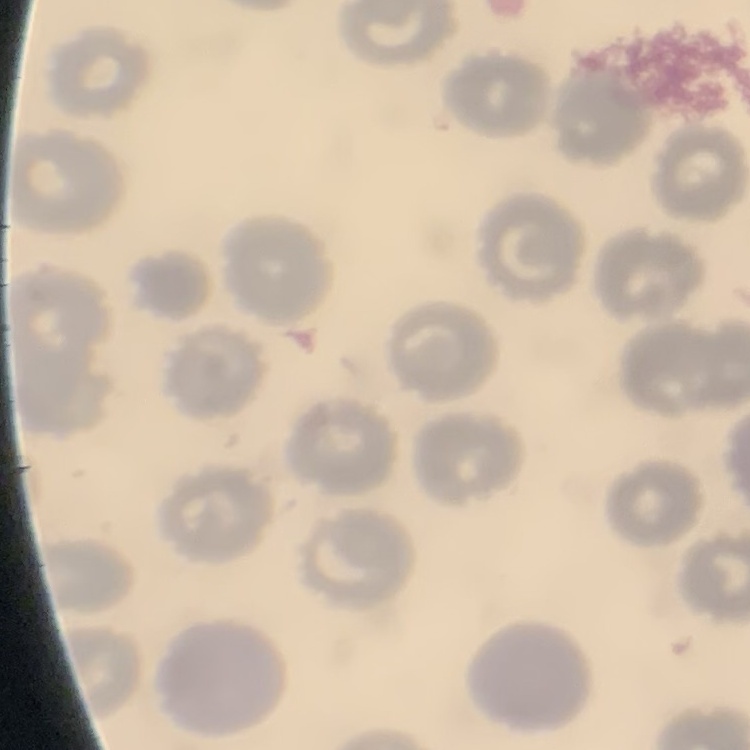 The red blood cells show no rouleaux formation. One tile cut from a larger photomicrograph. Field's or Giemsa stain. Thin peripheral smear.